Name the parasite shown.
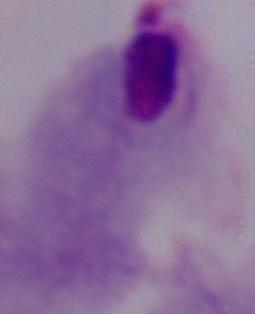
This is a trichomonad.

1000x magnification. Photomicrograph.